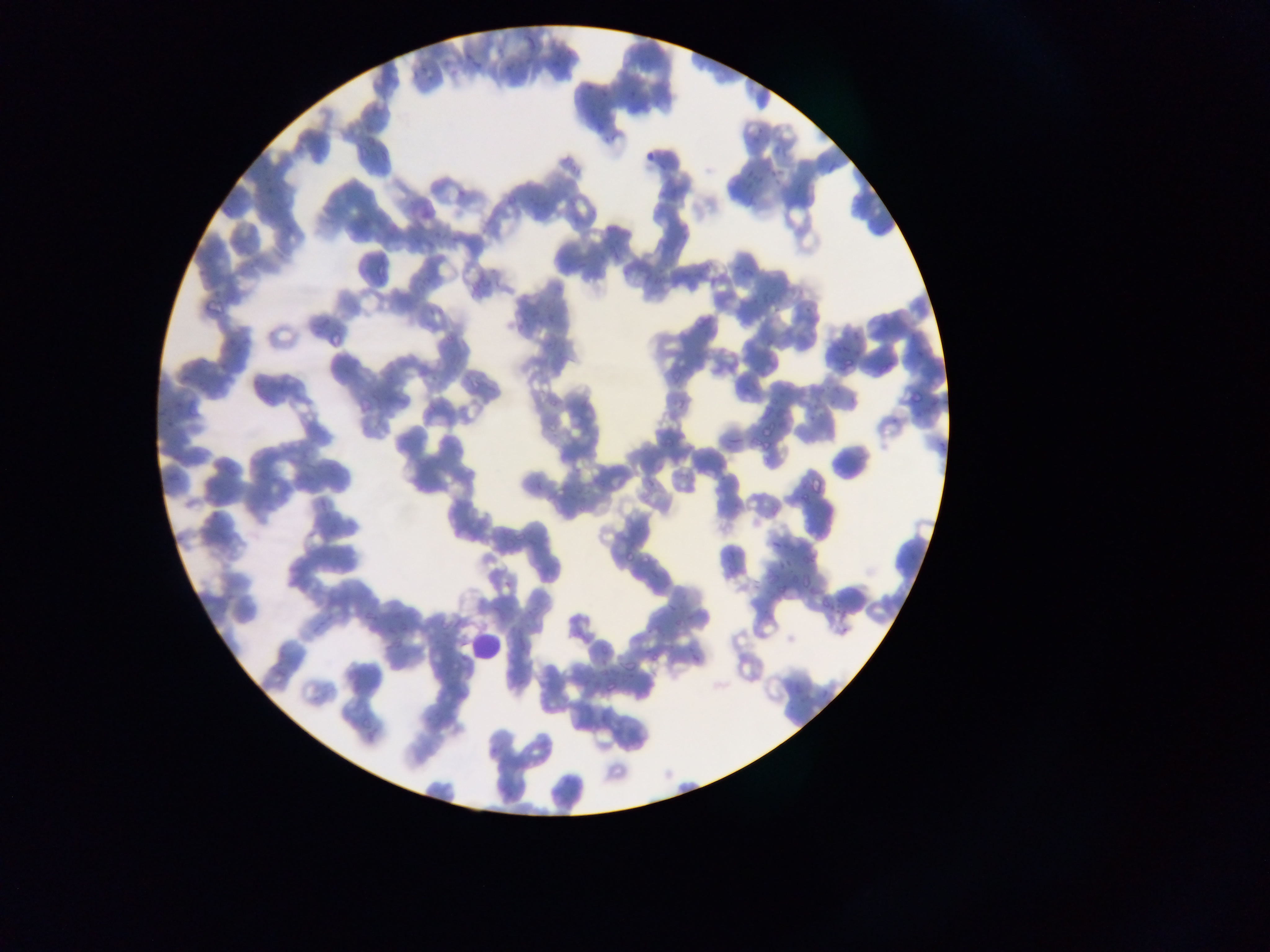

Approximate bounding boxes as left top right bottom in pixels. Malaria parasite locations: 523 32 538 51; 454 55 473 69; 414 62 428 79; 593 86 612 103; 577 87 589 98; 628 87 644 101; 643 151 659 163; 826 156 843 174; 742 167 755 179; 770 168 778 177; 269 189 289 210; 372 259 395 279; 195 267 213 281; 201 292 229 318; 427 303 439 318; 546 304 560 322; 443 331 454 345; 224 335 238 349; 180 353 203 382; 841 354 857 374; 219 361 226 372; 466 370 481 390; 363 385 386 403; 907 391 923 405; 184 395 203 419; 163 410 179 428; 757 424 776 438; 661 432 681 452; 728 436 739 450; 760 439 773 456; 301 470 315 486; 643 470 663 489; 807 473 827 493; 534 481 545 496; 315 496 330 513; 325 521 340 532; 770 533 784 550; 624 549 632 564; 649 564 658 579; 783 566 801 584; 798 573 819 588; 503 580 511 587; 817 594 831 611; 369 601 389 623; 665 603 676 617; 383 639 396 656; 650 648 665 665; 688 655 697 666; 622 656 637 675; 602 677 622 697. Leukocyte locations: 460 628 503 663. Sample from Ghana. Thin blood smear. One field of view. Photographed through a microscope with a mobile-phone camera. Image is 1270×952 pixels.